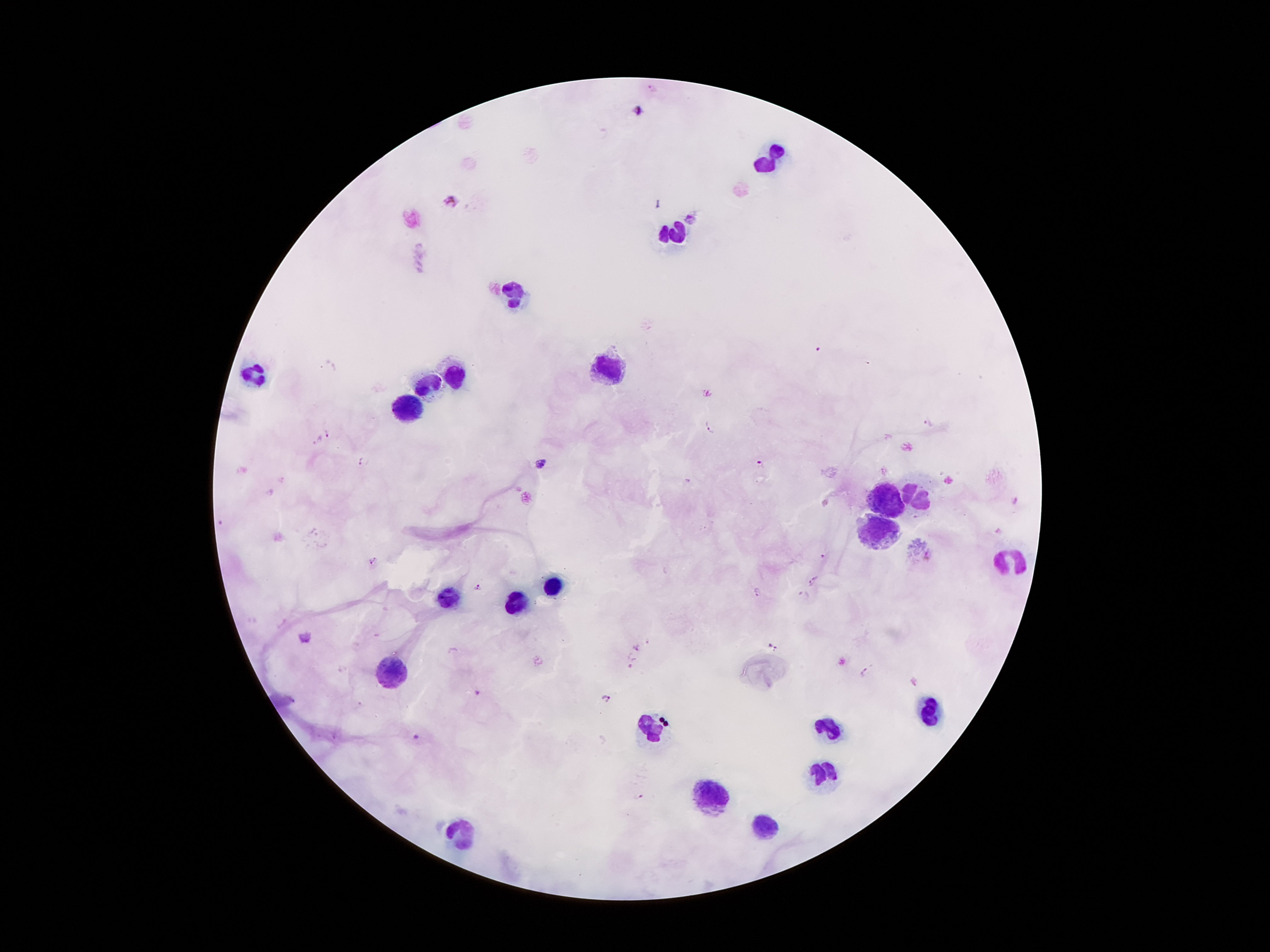
Approximate centers as {x, y} in pixels.
Summary:
  - Leukocyte locations: {769, 156}, {676, 237}, {513, 296}, {608, 366}, {251, 373}, {457, 373}, {431, 382}, {408, 408}, {886, 496}, {917, 496}, {875, 531}, {1012, 557}, {552, 585}, {445, 596}, {513, 604}, {396, 671}, {928, 718}, {826, 727}, {653, 732}, {823, 771}, {711, 797}, {767, 825}, {461, 827}
  - Malaria parasite locations: {654, 88}, {638, 111}, {451, 200}, {691, 216}, {818, 348}, {867, 362}, {928, 422}, {710, 426}, {327, 432}, {318, 442}, {362, 461}, {761, 464}, {541, 465}, {283, 480}, {1015, 501}, {220, 523}, {824, 556}, {928, 556}, {372, 559}, {814, 582}, {479, 588}, {757, 590}, {804, 594}, {306, 636}, {637, 647}, {774, 647}, {865, 672}, {914, 682}, {478, 693}, {609, 699}, {417, 736}, {639, 796}
  - Preparation: thick blood film
  - Field of view: one from this slide
  - Capture: smartphone camera through the microscope eyepiece
  - Stain: Giemsa
  - Image size: 1270×952 pixels
  - Patient malaria status: positive for Plasmodium falciparum
  - Magnification: 100x